Report the malaria status of this cell.
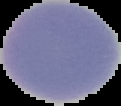
Uninfected.

image size = 121×106 pixels
image type = segmented cell region on a black background
preparation = thin blood smear